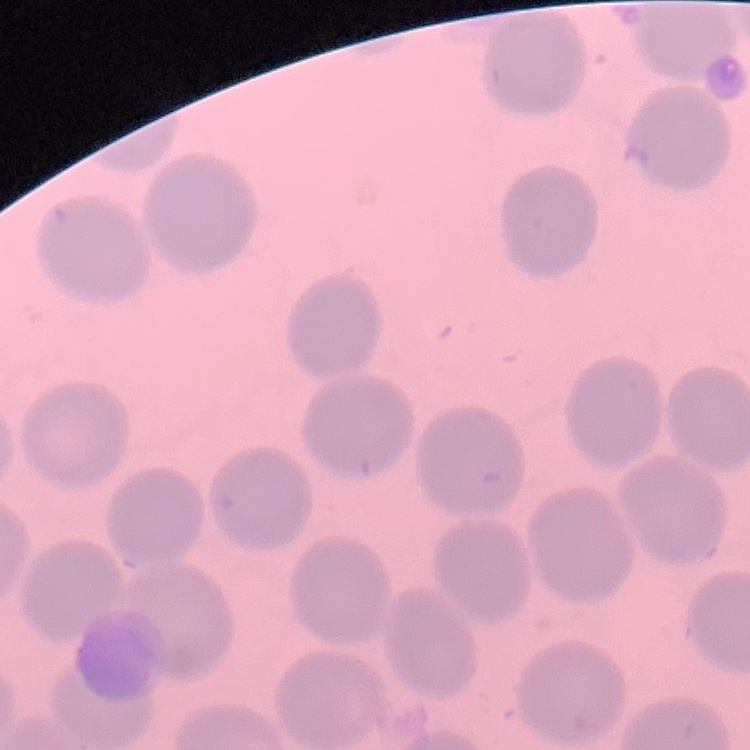 The red blood cells show no rouleaux formation. Thin blood smear. Square crop of a larger photomicrograph. Stained with either Field's or Giemsa.